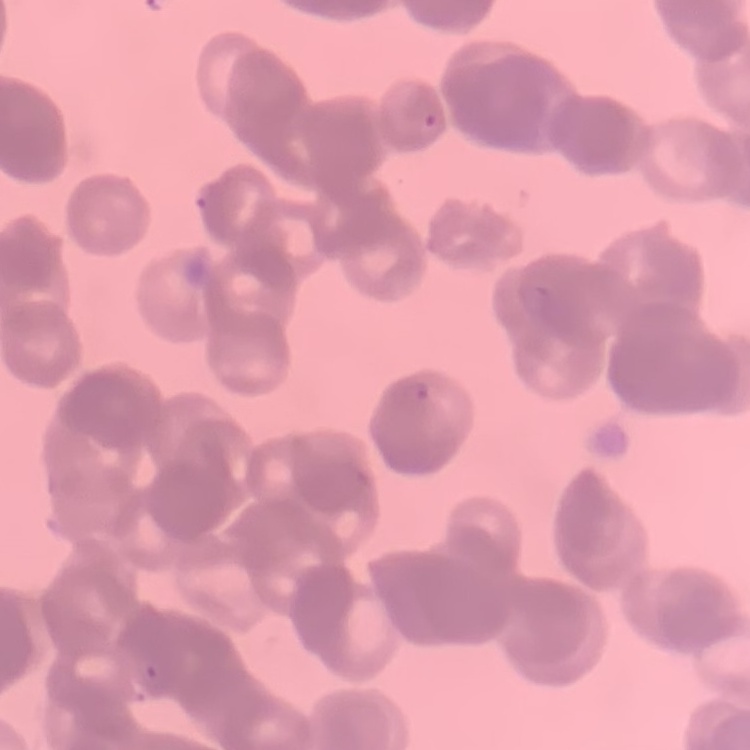
red_blood_cell_morphology: rouleaux formation
stain: Field's or Giemsa
image_type: one tile cut from a larger photomicrograph
preparation: thin peripheral smear